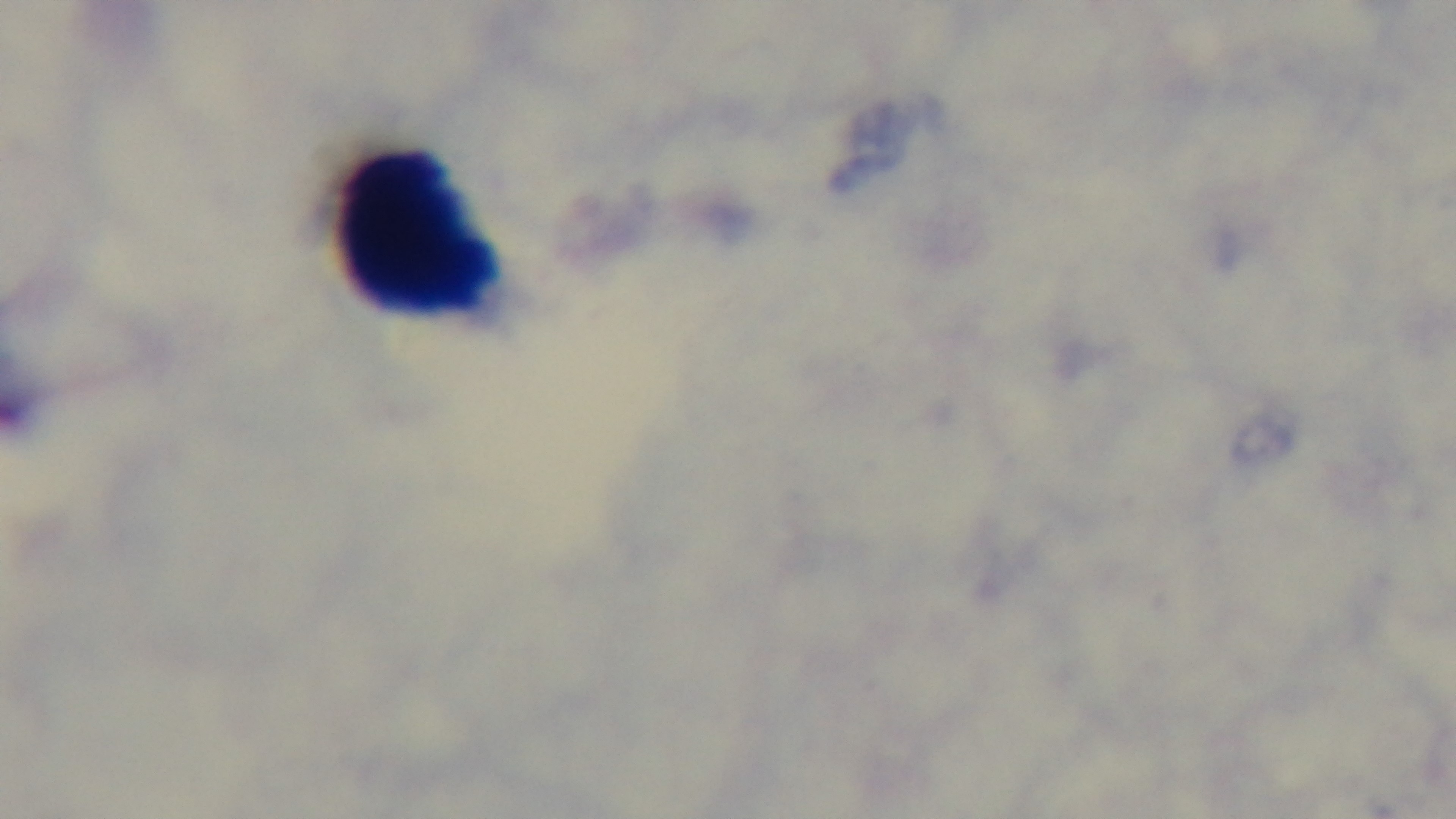
Oil-immersion objective, 100x. Mounted 4K digital camera. Preparation: thick blood film. Single field of view. Light microscopy. Malaria status: uninfected. Giemsa stain.